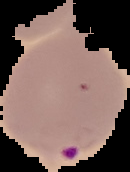
Summary:
  - Image size: 130×172 pixels
  - Image type: cell region segmented out of the field of view; surrounding area masked to black
  - Preparation: thin blood smear
  - Malaria status: parasitized